Give the position of every Plasmodium parasite.
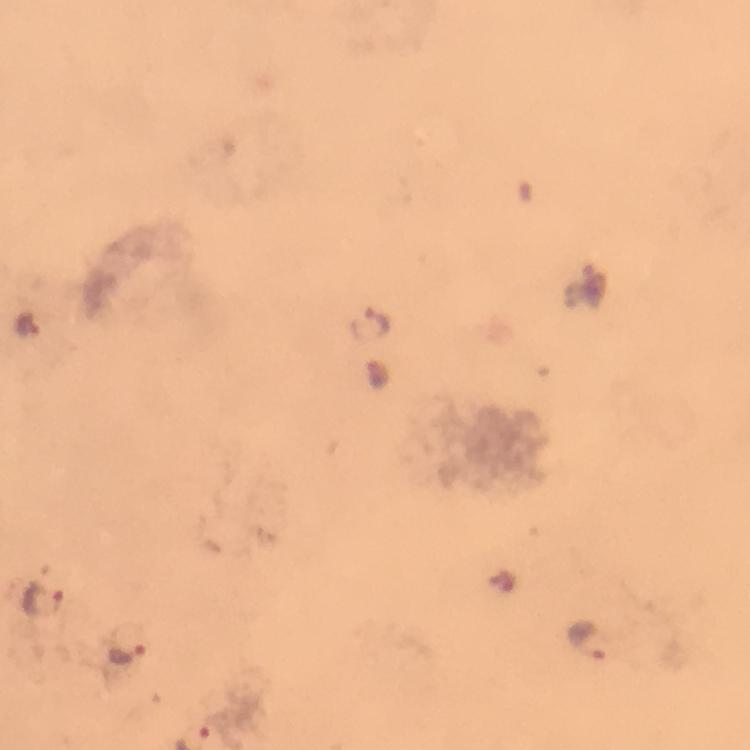
Approximate centers as {x, y} in pixels.
Plasmodium parasites: {372, 323}, {27, 325}, {44, 599}, {589, 640}, {129, 652}.

Thick blood film. Image is 750×750 pixels. From a diagnostic examination for malaria. Giemsa stain. Immersion oil was used. 100x magnification. A crop from one field of view. Smartphone photograph taken through a microscope.